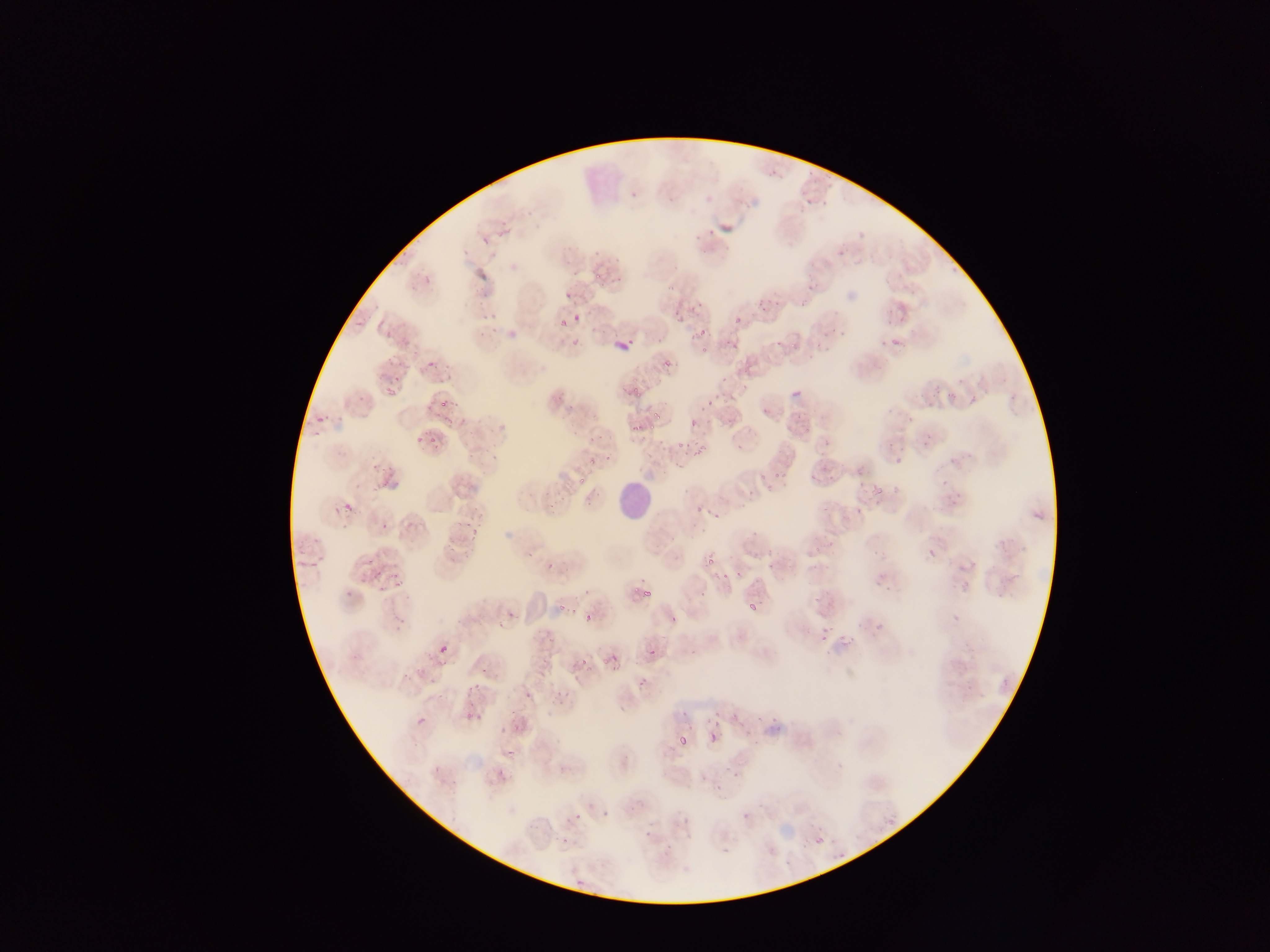

{
  "leukocyte_locations": "approximate bounding boxes as left top right bottom in pixels: 617 481 655 523",
  "field_of_view": "single",
  "country": "Ghana",
  "preparation": "thin blood film",
  "capture": "mobile-phone photograph through a microscope",
  "image_size": "1270×952 pixels",
  "malaria_parasite_locations": "approximate bounding boxes as left top right bottom in pixels (subset; some below the resolvable size): 631 191 638 199; 690 224 712 243; 613 276 622 285; 563 292 570 300; 730 310 744 324; 572 315 581 323; 554 318 565 331; 693 327 709 337; 566 333 579 343; 613 336 629 347; 775 336 785 347; 731 337 743 354; 699 347 707 354; 662 351 680 367; 426 360 436 369; 387 379 399 393; 624 382 645 400; 439 399 449 410; 649 400 672 418; 703 402 711 409; 725 411 737 423; 316 415 325 424; 689 419 697 427; 629 422 642 433; 676 440 691 450; 734 441 747 453; 600 445 616 462; 690 451 708 459; 894 457 903 465; 819 459 829 473; 376 469 391 486; 871 484 884 499; 874 487 884 497; 696 499 705 519; 341 503 353 513; 712 507 728 516; 462 518 472 529; 380 520 390 531; 461 541 473 553; 524 548 535 562; 926 549 935 558; 705 557 714 566; 547 559 557 569; 722 561 734 576; 766 562 774 570; 365 567 379 580; 389 576 404 591; 628 582 640 596; 640 589 650 605; 555 597 567 610; 510 602 522 618; 748 603 757 613; 668 612 679 628; 584 613 593 622; 876 617 885 633; 799 627 808 636; 820 631 829 641; 438 645 448 655; 649 648 657 657; 575 652 602 671; 607 653 623 673; 522 675 544 707; 752 697 772 723; 464 703 481 717; 710 706 726 716; 416 716 427 726; 709 729 720 744; 676 732 691 749; 496 769 506 779; 572 812 581 821; 815 836 824 845"
}